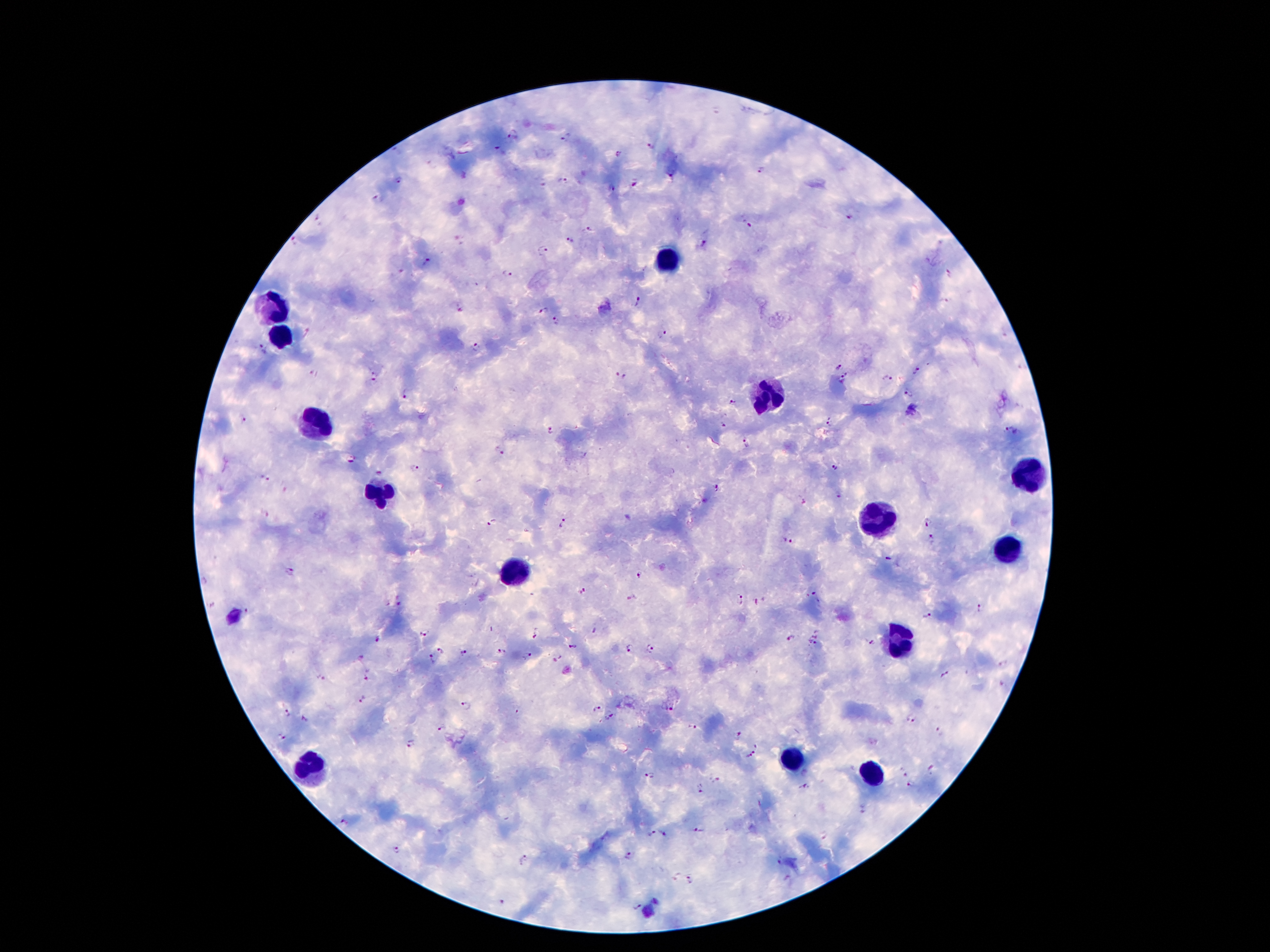

100x magnification. Photographed through the microscope eyepiece with a smartphone camera. Giemsa-stained preparation. Thick blood smear. Patient malaria status: positive for Plasmodium falciparum. Image is 1270×952 pixels. One field from this slide.